Outline every trophozoite.
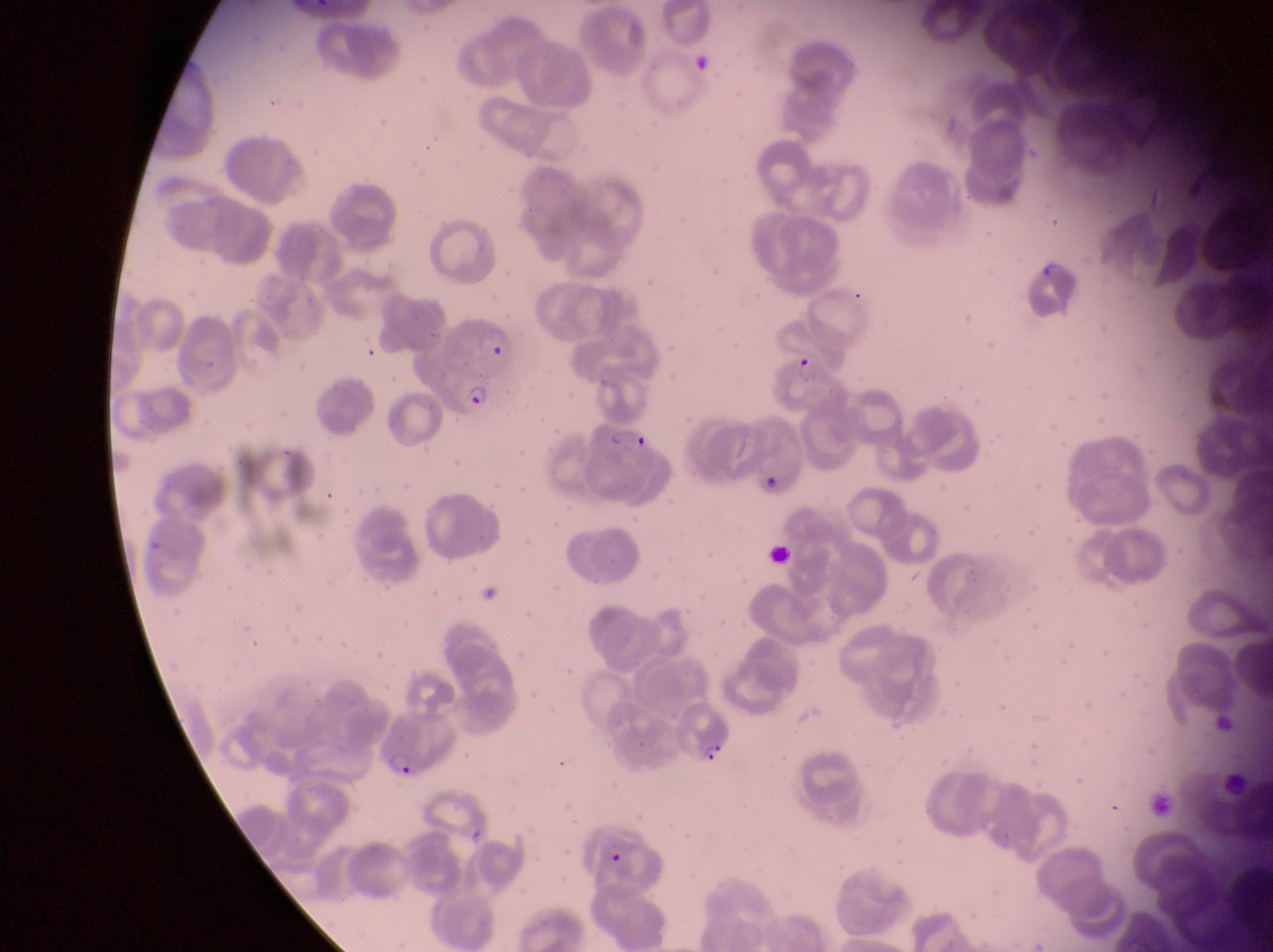

Approximate bounding boxes as [left, top, right, bottom] in pixels.
Trophozoites: [594, 835, 626, 861].

country = Uganda
capture = smartphone photograph through the eyepiece of an Olympus CX-23 microscope
field of view = single
magnification = 1000x
image size = 1273×952 pixels
parasitised red blood cell locations = approximate bounding boxes as [left, top, right, bottom] in pixels: [452, 309, 522, 369], [778, 354, 852, 421], [430, 362, 504, 419], [590, 425, 660, 501], [679, 699, 734, 771], [375, 712, 460, 780]
preparation = thin blood smear